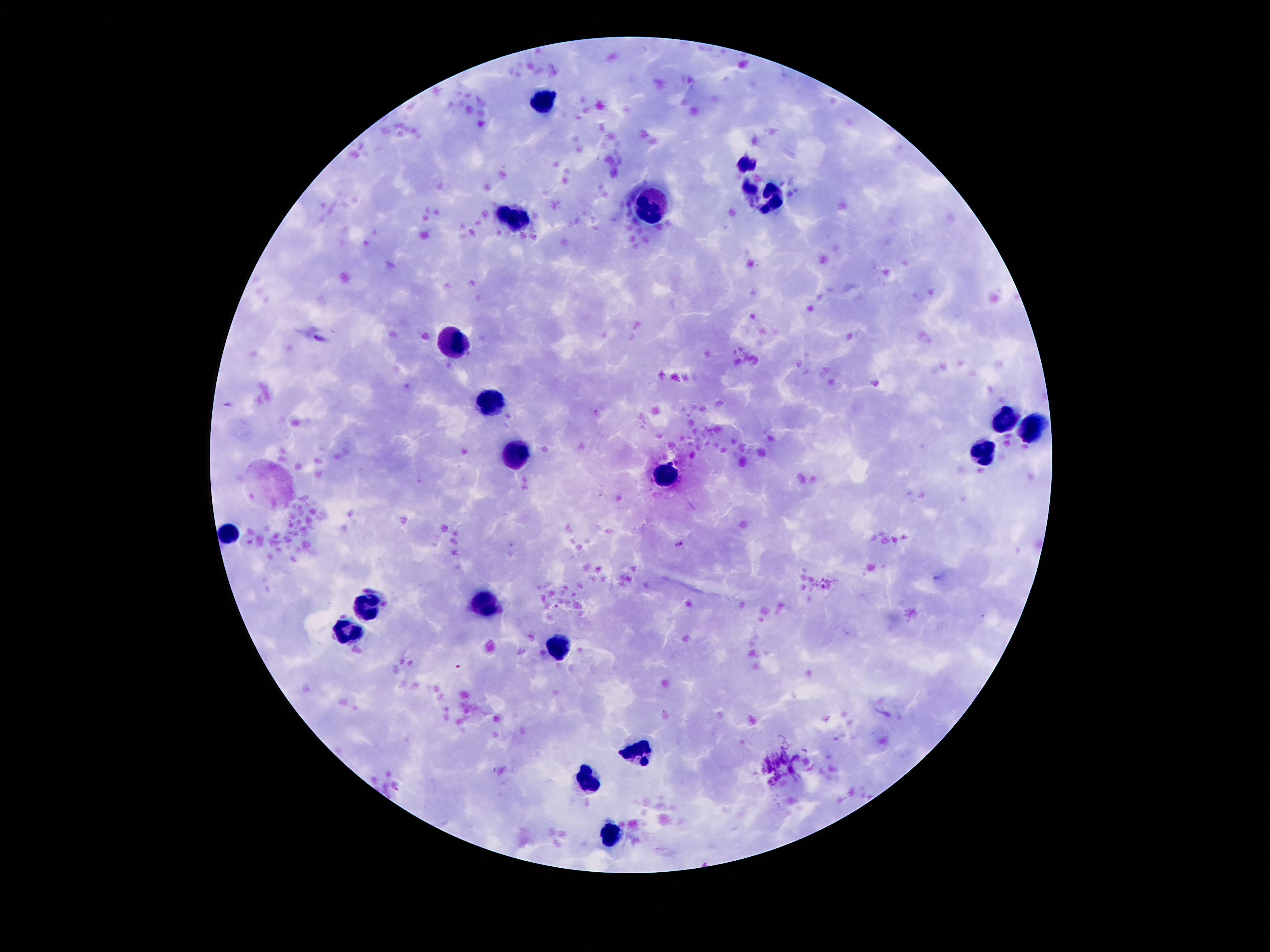
Approximate centers as [x, y] in pixels.
Summary:
  - Leukocyte locations: [543, 102], [762, 193], [647, 205], [514, 217], [452, 342], [491, 404], [1004, 418], [1028, 428], [983, 453], [514, 457], [666, 473], [227, 535], [483, 604], [366, 609], [342, 633], [557, 650], [639, 750], [588, 783], [610, 836]
  - Capture: smartphone camera through the microscope eyepiece
  - Preparation: thick peripheral-blood smear
  - Patient malaria status: negative
  - Field of view: single
  - Image size: 1270×952 pixels
  - Stain: Giemsa
  - Magnification: 100x